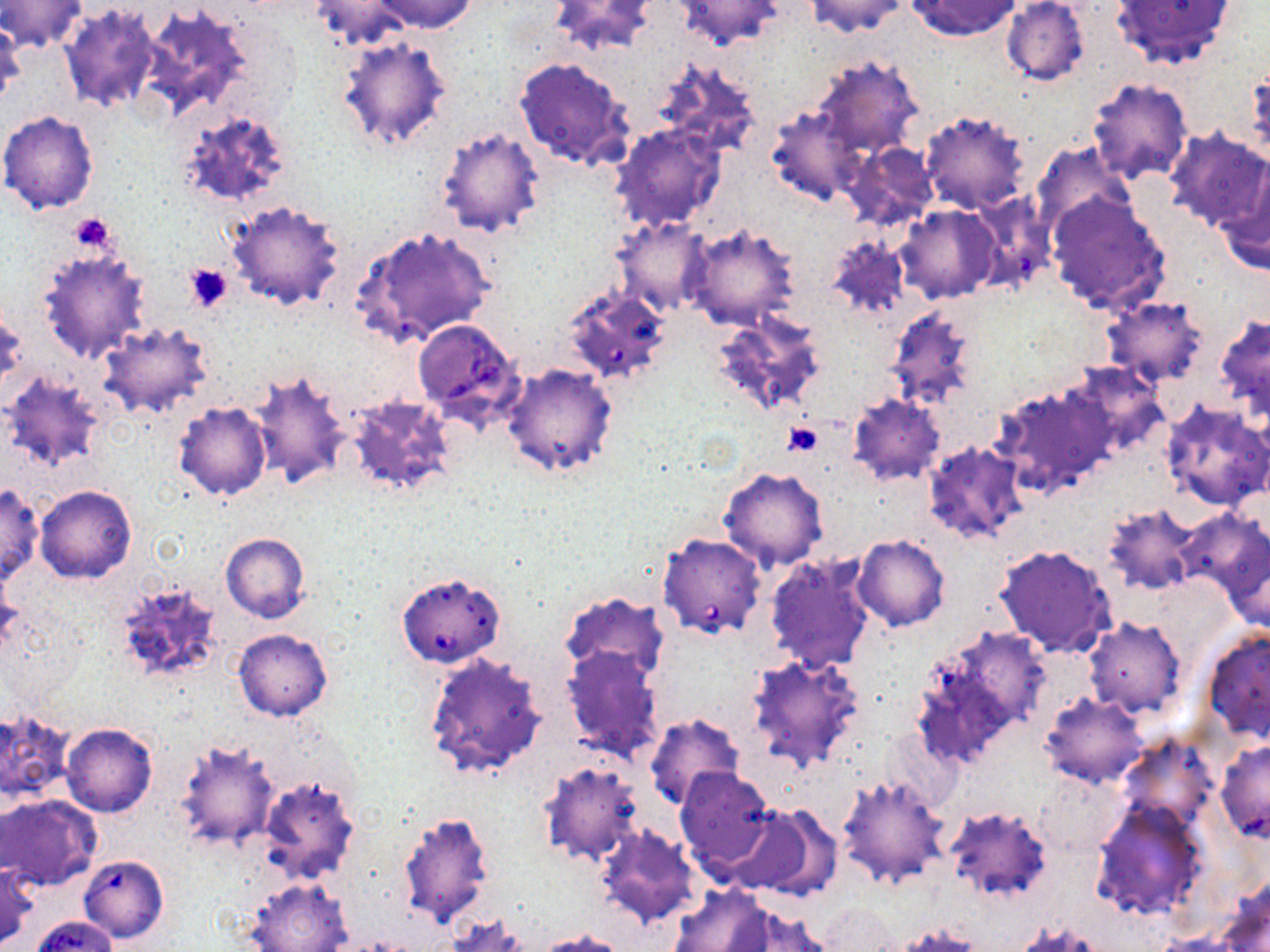
Approximate bounding boxes as (x1,y1)-(x2,y2) corner pairs in pixels. Babesia divergens-infected red blood cell locations: (412,319)-(523,424), (657,532)-(767,639), (395,571)-(506,668), (78,855)-(169,944). Uninfected red blood cell locations: (370,0)-(478,34), (804,0)-(909,37), (906,0)-(1022,40), (0,1)-(87,55), (310,1)-(418,51), (548,1)-(659,57), (671,1)-(786,51), (1001,1)-(1089,87), (1113,1)-(1235,72), (57,2)-(162,112), (135,2)-(259,123), (0,18)-(24,111), (334,34)-(456,152), (811,54)-(923,161), (514,56)-(634,172), (650,57)-(763,158), (1245,61)-(1270,162), (1085,78)-(1192,186), (767,105)-(865,206), (0,110)-(100,215), (179,110)-(293,210), (919,110)-(1030,214), (610,122)-(728,233), (433,124)-(547,240), (1164,127)-(1269,232), (840,141)-(938,232), (1033,143)-(1138,239), (1217,161)-(1270,276), (1048,194)-(1170,314), (227,200)-(346,311), (894,205)-(1000,304), (610,216)-(713,316), (683,221)-(800,331), (351,226)-(494,348), (823,235)-(910,321), (36,246)-(152,363), (569,282)-(667,380), (1098,296)-(1208,387), (882,306)-(979,410), (1,308)-(26,397), (709,309)-(827,416), (1215,314)-(1270,418), (97,320)-(214,420), (501,363)-(620,478), (1064,364)-(1171,460), (247,368)-(353,492), (3,372)-(109,473), (993,382)-(1114,499), (848,394)-(946,486), (345,395)-(457,497), (173,401)-(271,502), (1160,401)-(1269,511), (922,441)-(1032,545), (718,466)-(829,571), (0,482)-(44,586), (36,485)-(137,584), (1101,503)-(1201,595), (1180,507)-(1268,610), (221,532)-(310,623), (852,534)-(950,631), (1219,535)-(1270,635), (993,542)-(1118,658), (764,552)-(876,674), (109,580)-(229,686), (558,591)-(671,684), (1084,619)-(1187,719), (912,626)-(1050,770), (1201,626)-(1270,743), (233,629)-(333,721), (560,644)-(665,763), (423,650)-(548,783), (746,652)-(866,772), (1039,692)-(1149,788), (0,706)-(75,802), (642,713)-(746,811), (61,723)-(157,817), (172,738)-(279,852), (1122,738)-(1215,826), (1215,740)-(1269,843), (536,760)-(643,865), (674,766)-(775,875), (1037,770)-(1121,857), (838,773)-(952,890), (253,774)-(360,885), (2,794)-(101,890), (1090,799)-(1208,921), (730,804)-(837,899), (943,806)-(1055,903), (398,808)-(496,929), (594,824)-(704,930), (0,862)-(37,949), (243,875)-(352,952), (668,886)-(773,951), (719,906)-(836,952), (30,914)-(119,952), (442,915)-(530,952), (1016,921)-(1104,951), (890,923)-(982,951), (534,929)-(631,952). Platelet locations: (67,214)-(116,253), (185,262)-(235,313), (782,420)-(824,457). Slide-level diagnosis: Babesia divergens. Light microscopy. One field of a larger specimen. May-Grünwald-Giemsa stain. Image is 1270×952 pixels. Thin blood smear. 1000x magnification.